Classify this cell by malaria status.
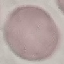

It is uninfected.

Giemsa-stained preparation. Thin smear of blood. Photographed with a smartphone camera at the microscope eyepiece. Cell patch, automatically extracted from a larger field of view and resized to 64 × 64 pixels.